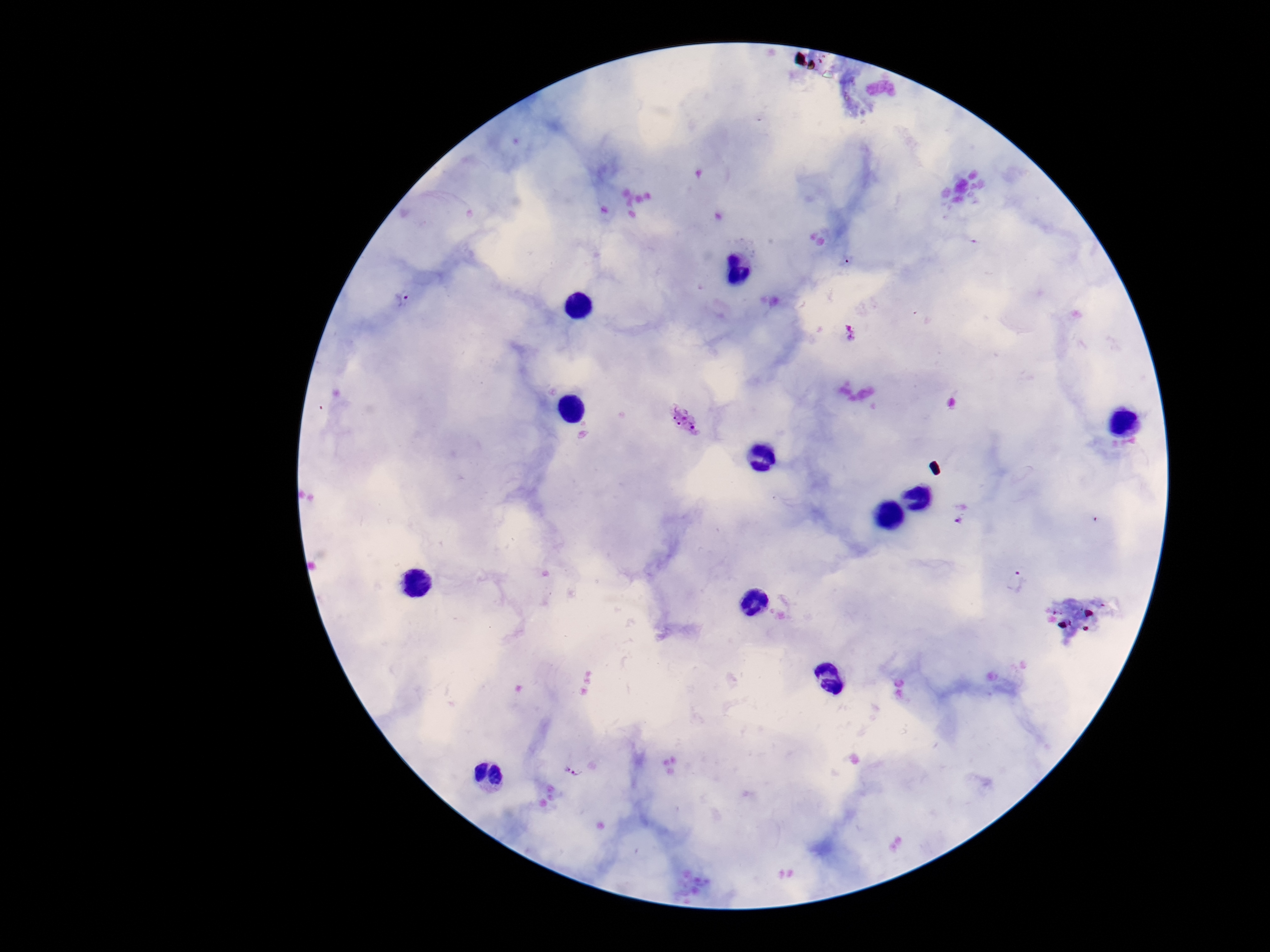
Approximate object centers, in pixels from the top-left corner.
Summary:
  - Plasmodium parasite locations: (x=403, y=298), (x=850, y=333), (x=684, y=419), (x=960, y=513), (x=1016, y=581), (x=573, y=767)
  - Magnification: 100x
  - Image size: 1270×952 pixels
  - Stain: Giemsa
  - Field of view: single
  - Patient malaria status: infected
  - Preparation: thick blood film
  - Capture: smartphone camera through the microscope eyepiece